Report the malaria status of this cell.
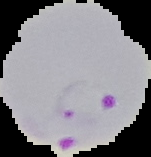
It is parasitized.

Image is 151×157 pixels. From a thin blood film. Cell region segmented out of the field of view; the surrounding area is masked to black.